Report the malaria status of this cell.
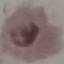
Parasitized.

Summary:
  - Capture: smartphone through the microscope eyepiece
  - Stain: Giemsa
  - Image type: automatically extracted cell patch, resized to 64 × 64 pixels
  - Preparation: thin smear